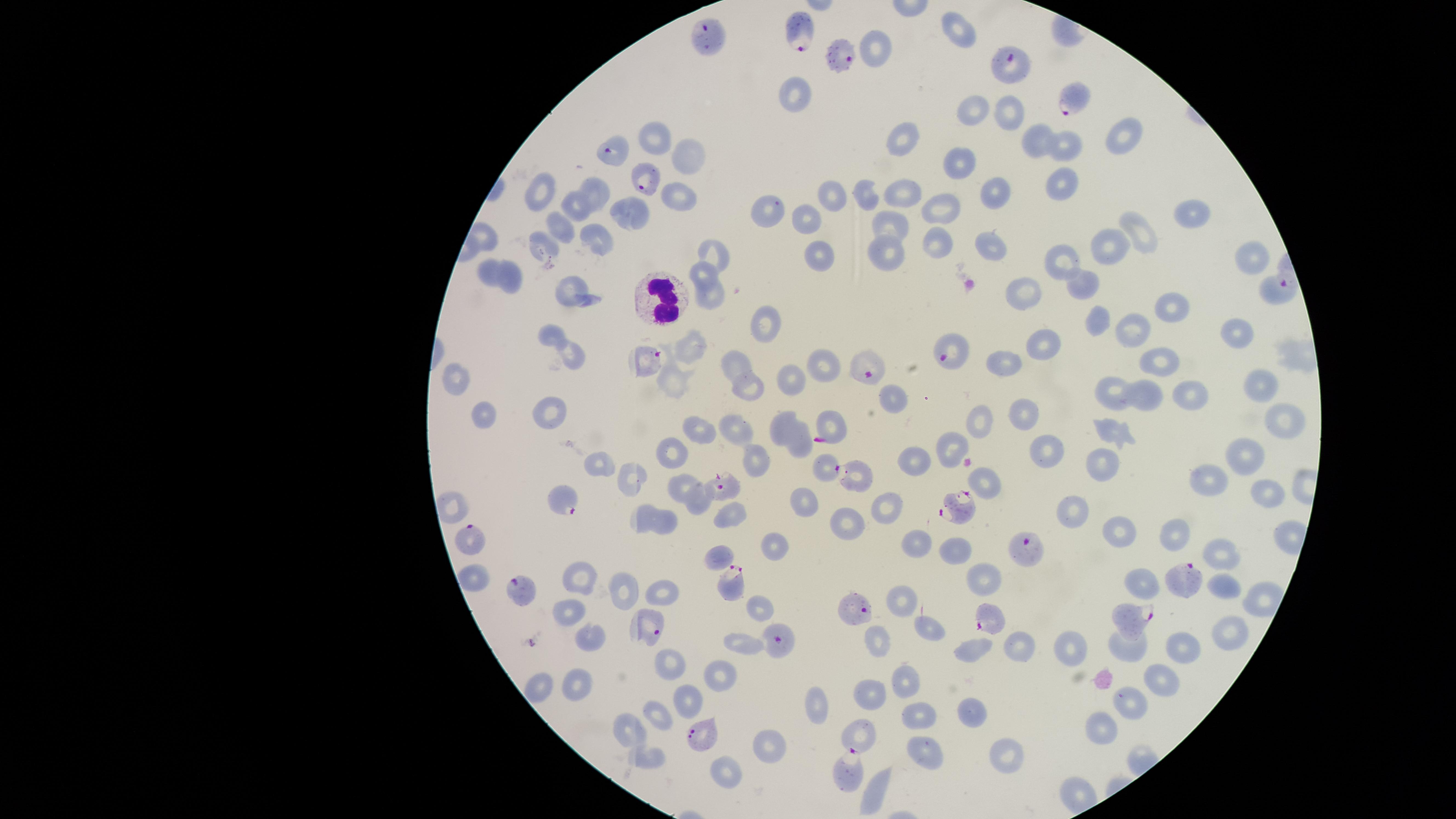 Approximate marker points as (x, y) in pixels. Parasitized red blood cells: (710, 33), (798, 33), (845, 53), (1011, 64), (1077, 98), (619, 152), (645, 177), (1272, 288), (955, 355), (649, 361), (872, 366), (828, 468), (722, 488), (566, 498), (959, 507), (465, 538), (1030, 546), (1182, 578), (517, 586), (732, 586), (854, 605), (1135, 617), (991, 618), (650, 624), (778, 642), (701, 736), (846, 768). Uninfected red blood cells: (956, 32), (876, 47), (795, 98), (974, 109), (1004, 114), (651, 137), (1125, 137), (904, 143), (1035, 143), (1065, 147), (688, 156), (960, 163), (1063, 187), (593, 192), (995, 193), (866, 194), (533, 196), (900, 196), (831, 197), (674, 200), (573, 205), (944, 211), (629, 212), (767, 212), (1190, 217), (807, 221), (889, 222), (558, 226), (1135, 236), (591, 241), (541, 246), (934, 246), (1105, 248), (992, 249), (887, 250), (714, 256), (1247, 256), (817, 258), (1065, 263), (488, 275), (702, 275), (513, 276), (567, 284), (1078, 285), (1025, 294), (706, 298), (1167, 310), (1092, 319), (763, 323), (1129, 329), (550, 335), (1236, 335), (1049, 345), (690, 347), (570, 359), (1003, 363), (731, 364), (823, 364), (1156, 369), (787, 381), (455, 382), (676, 382), (1262, 383), (745, 391), (1113, 395), (1143, 399), (1188, 400), (888, 404), (552, 415), (481, 416), (1021, 418), (828, 422), (1287, 423), (777, 425), (974, 426), (733, 428), (696, 430), (1109, 430), (796, 446), (948, 448), (674, 452), (1245, 453), (1046, 455), (915, 459), (600, 460), (756, 462), (1098, 465), (633, 478), (852, 482), (680, 484), (1210, 484), (983, 487), (1263, 489), (807, 505), (455, 506), (695, 507), (882, 511), (1074, 513), (637, 516), (730, 518), (667, 523), (851, 523), (1119, 533), (1174, 535), (915, 539), (773, 551), (956, 552), (1222, 554), (717, 560), (475, 574), (580, 578), (983, 580), (1222, 586), (624, 589), (1143, 589), (663, 596), (896, 606), (759, 608), (569, 609), (928, 629), (1231, 630), (593, 637), (738, 644), (1130, 644), (1181, 644), (874, 647), (1022, 647), (1070, 647), (977, 651), (670, 667), (724, 677), (577, 682), (1159, 682), (902, 685), (544, 688), (874, 695), (685, 697), (1135, 702), (816, 708), (971, 715), (920, 717), (661, 719), (1101, 729), (629, 730), (862, 734), (772, 740), (926, 748), (996, 752), (650, 761), (725, 772), (874, 791). White blood cells: (659, 301). Species: Plasmodium falciparum. One field of view of the specimen. Thin smear of blood. Image is 1456×819 pixels. Photographed with a smartphone camera through the microscope eyepiece. Giemsa-stained preparation. The visible region is circular. Presence: malaria parasites seen.